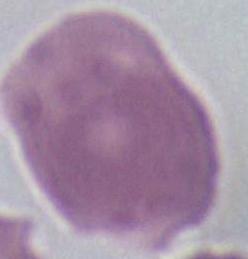
Photomicrograph. A red blood cell is seen. 1000x magnification.